Give the extent of all Plasmodium malariae-infected red blood cells.
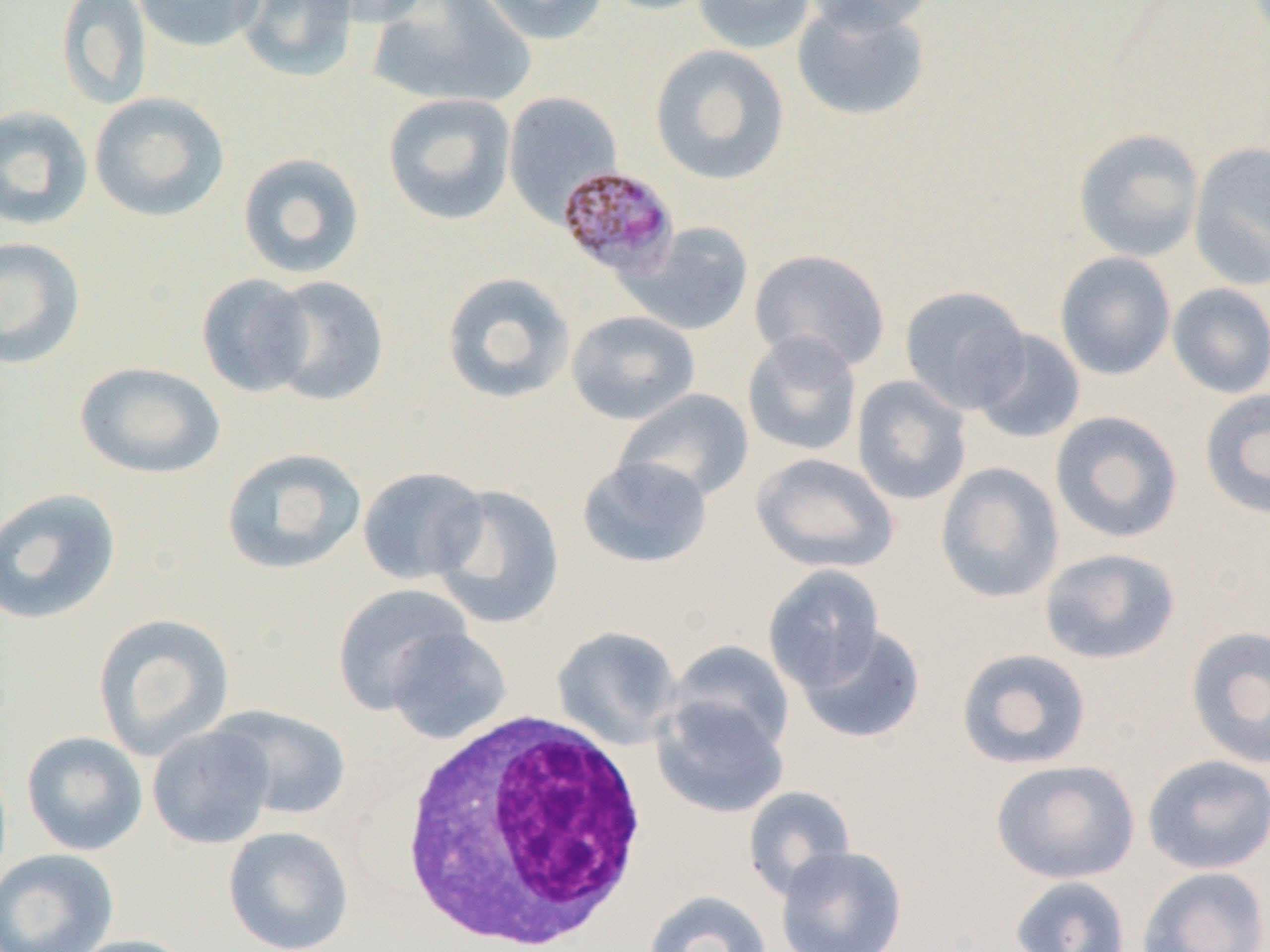
Approximate bounding boxes as (x1, y1, x2, y2) in pixels.
Plasmodium malariae-infected red blood cells: (558, 164, 681, 280).

slide-level diagnosis = Plasmodium malariae
magnification = 1000x
white blood cell locations = approximate bounding boxes as (x1, y1, x2, y2) in pixels: (392, 708, 651, 952)
preparation = thin blood smear
modality = optical microscopy
uninfected red blood cell locations = approximate bounding boxes as (x1, y1, x2, y2) in pixels: (56, 0, 152, 111), (132, 0, 266, 53), (232, 0, 360, 83), (305, 0, 434, 28), (367, 0, 536, 110), (475, 0, 610, 45), (595, 0, 721, 16), (692, 0, 816, 54), (800, 0, 936, 34), (792, 2, 930, 122), (650, 44, 790, 185), (89, 91, 230, 222), (503, 91, 623, 225), (382, 92, 516, 226), (0, 105, 94, 231), (1073, 128, 1205, 262), (1188, 141, 1270, 290), (237, 151, 366, 280), (621, 222, 754, 336), (0, 236, 87, 370), (749, 248, 891, 373), (1055, 251, 1176, 381), (441, 271, 576, 405), (196, 273, 316, 398), (262, 275, 390, 406), (1167, 283, 1270, 398), (899, 285, 1032, 415), (566, 310, 700, 425), (742, 330, 862, 457), (970, 330, 1085, 444), (74, 361, 226, 479), (852, 375, 972, 506), (614, 388, 754, 504), (1199, 388, 1270, 520), (1050, 410, 1183, 544), (220, 447, 366, 575), (751, 452, 900, 574), (576, 456, 713, 570), (935, 462, 1065, 604), (356, 466, 490, 585), (430, 484, 565, 629), (0, 487, 122, 626), (1039, 548, 1181, 665), (762, 564, 886, 692), (331, 583, 474, 715), (93, 613, 235, 761), (552, 624, 683, 751), (795, 624, 926, 744), (1184, 625, 1270, 770), (383, 626, 513, 745), (668, 640, 796, 755), (955, 648, 1092, 770), (651, 696, 790, 819), (206, 705, 353, 821), (147, 723, 276, 849), (21, 731, 148, 856), (1142, 754, 1270, 874), (991, 759, 1140, 884), (743, 786, 857, 900), (223, 826, 354, 952), (775, 844, 908, 952), (0, 849, 118, 952), (1137, 866, 1269, 952), (1010, 875, 1131, 952), (642, 890, 773, 952), (63, 934, 195, 952)
field of view = one of a larger specimen
image size = 1270×952 pixels